Classify this cell by malaria status.
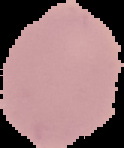

It is uninfected.

From a thin blood smear. Image is 124×148 pixels. Segmented cell region on a black background.